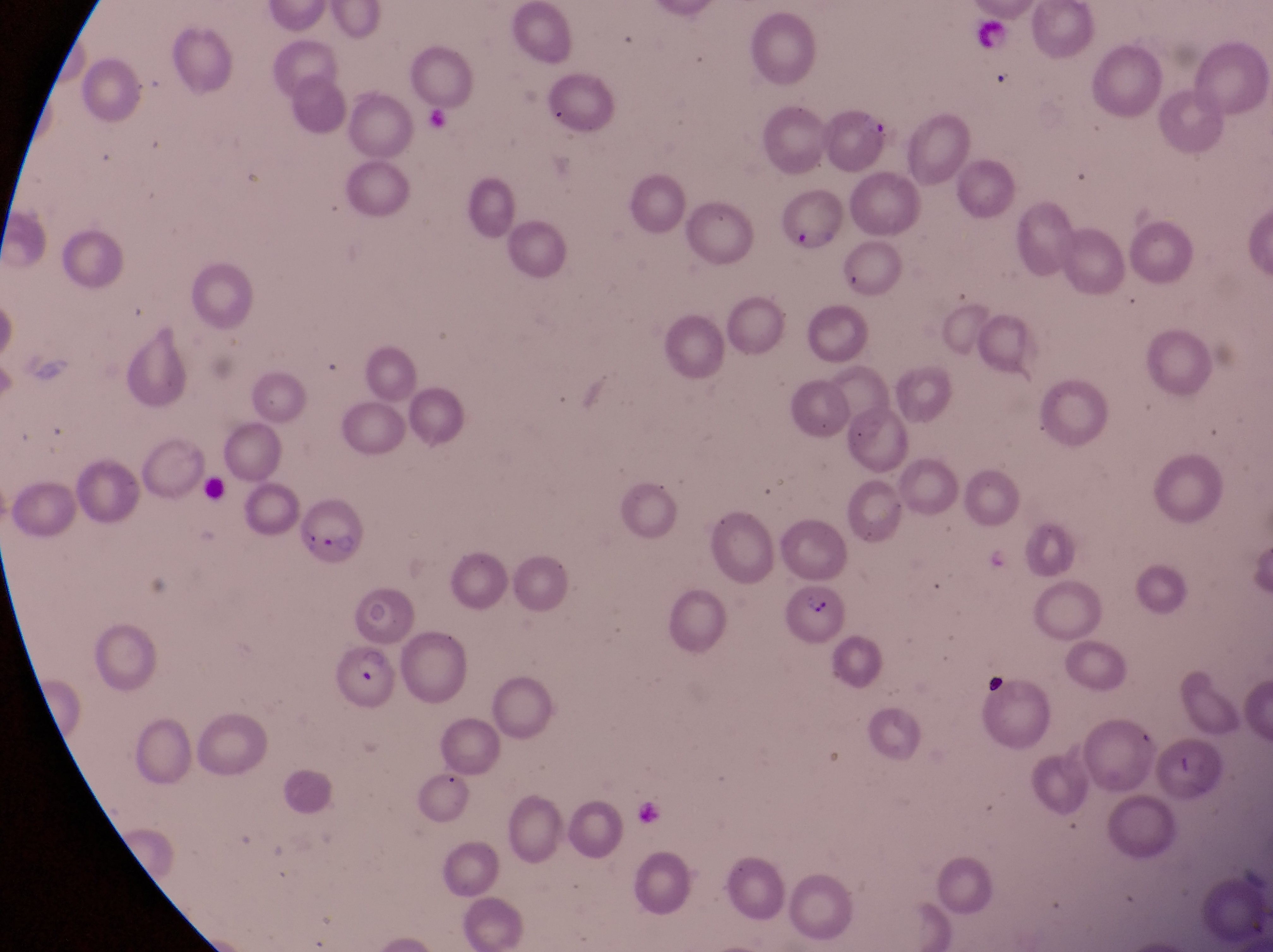 Approximate bounding boxes as left top right bottom in pixels. Leukocyte locations: 974 16 1016 59. Parasitised red blood cell locations: 302 494 369 564; 786 584 849 641; 332 644 399 709. Image is 1273×952 pixels. One field of view. Photographed through the eyepiece of an Olympus CX-23 microscope with a smartphone camera. Magnification of 1000x. Sample from Uganda. Thin blood smear.